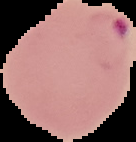
Segmented cell region on a black background. Image is 136×142 pixels. From a thin blood film. Malaria status: parasitized.